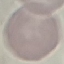

Result: negative for malaria parasites. Giemsa-stained preparation. Thin smear of blood. Cell patch, automatically extracted from a larger field of view and resized to 64 × 64 pixels. Acquired by smartphone through the microscope eyepiece.